Give the extent of all uninfected red blood cells.
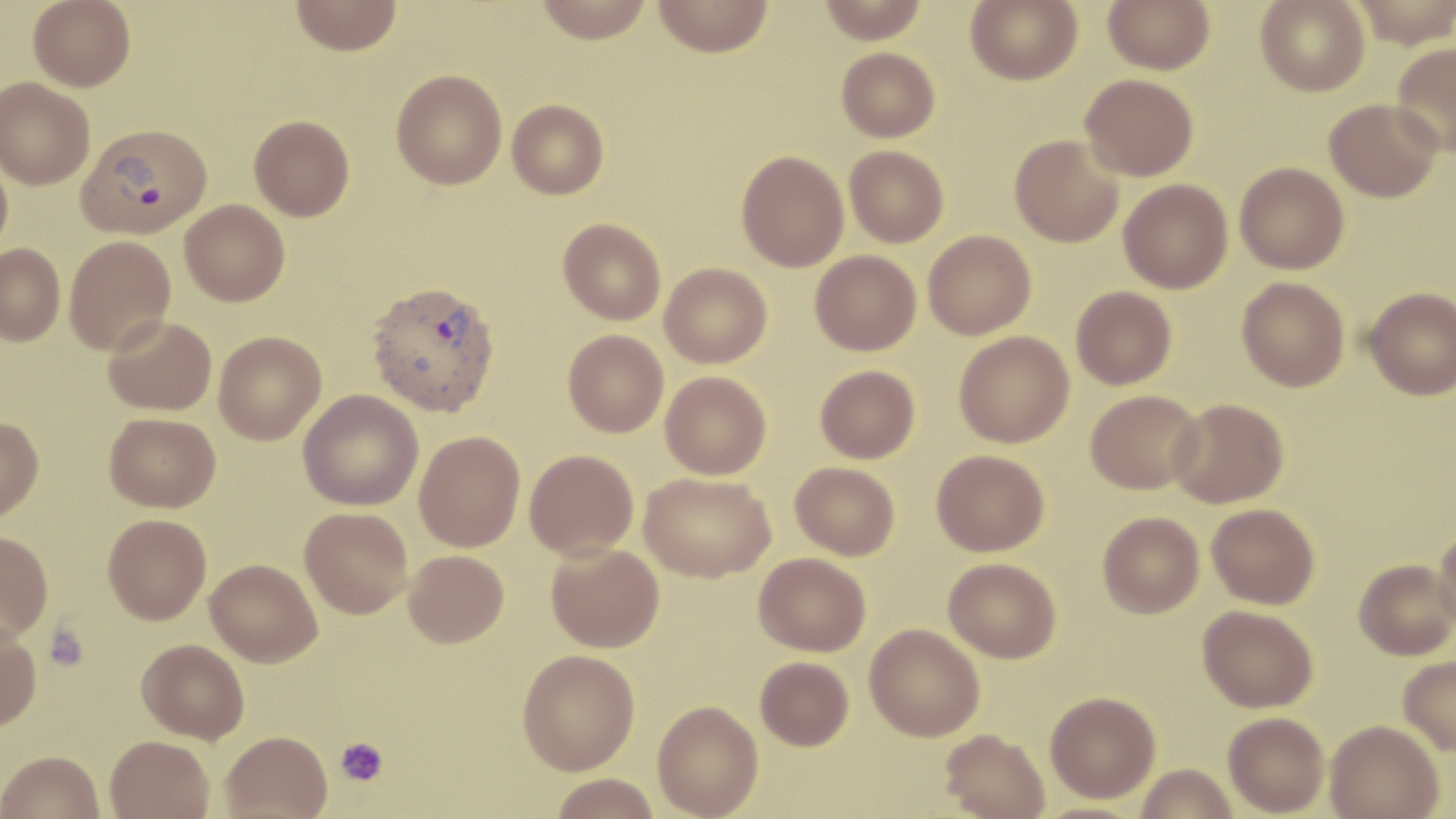

Approximate bounding boxes as (x1, y1, x2, y2) in pixels.
Uninfected red blood cells: (28, 0, 135, 91), (290, 0, 403, 55), (533, 0, 656, 43), (652, 0, 775, 56), (817, 0, 930, 43), (964, 0, 1083, 86), (1103, 0, 1215, 74), (1256, 0, 1369, 96), (1348, 0, 1456, 49), (1392, 42, 1456, 157), (836, 47, 940, 142), (391, 69, 507, 190), (1080, 73, 1199, 180), (0, 77, 95, 189), (1324, 98, 1443, 202), (507, 99, 609, 199), (249, 114, 355, 221), (1009, 135, 1124, 247), (844, 145, 949, 247), (0, 148, 13, 258), (736, 150, 849, 272), (1234, 162, 1349, 274), (1119, 179, 1233, 293), (180, 199, 290, 305), (558, 218, 666, 325), (923, 229, 1036, 339), (64, 236, 176, 355), (0, 244, 65, 346), (810, 250, 921, 355), (660, 262, 772, 368), (1237, 276, 1350, 392), (1071, 286, 1176, 389), (1364, 287, 1456, 400), (103, 315, 217, 415), (563, 329, 668, 437), (954, 330, 1074, 447), (214, 331, 326, 444), (815, 365, 920, 463), (660, 371, 771, 479), (297, 389, 423, 510), (1085, 389, 1204, 494), (1168, 398, 1289, 508), (104, 412, 221, 512), (0, 416, 44, 521), (414, 431, 525, 552), (524, 449, 639, 560), (931, 449, 1049, 556), (790, 461, 900, 560), (639, 472, 775, 582), (1206, 503, 1320, 609), (300, 507, 412, 618), (1098, 511, 1204, 618), (103, 514, 212, 625), (1434, 527, 1456, 632), (0, 531, 53, 642), (546, 542, 664, 653), (403, 550, 509, 648), (753, 553, 871, 656), (943, 557, 1061, 663), (205, 558, 322, 666), (1354, 559, 1455, 659), (1198, 604, 1318, 712), (0, 623, 41, 732), (864, 623, 985, 741), (137, 639, 249, 742), (516, 649, 640, 775), (1398, 655, 1456, 756), (755, 656, 854, 750), (1045, 691, 1161, 803), (652, 700, 764, 819), (1223, 712, 1329, 816), (1325, 719, 1444, 819), (940, 728, 1050, 819), (220, 730, 333, 818), (104, 735, 214, 819), (0, 750, 104, 819), (1136, 763, 1238, 819), (548, 773, 661, 819).

slide_level_diagnosis: Plasmodium vivax
magnification: 1000x
stain: May-Grünwald-Giemsa
field_of_view: single
image_size: 1456×819 pixels
plasmodium_vivax_infected_red_blood_cell_locations: 'approximate bounding boxes as (x1, y1, x2, y2) in pixels: (77, 122, 212, 238), (367, 280, 500, 418)'
platelet_locations: 'approximate bounding boxes as (x1, y1, x2, y2) in pixels: (45, 624, 89, 670), (335, 737, 389, 787)'
preparation: thin blood film
modality: optical microscopy